Name the parasite shown.
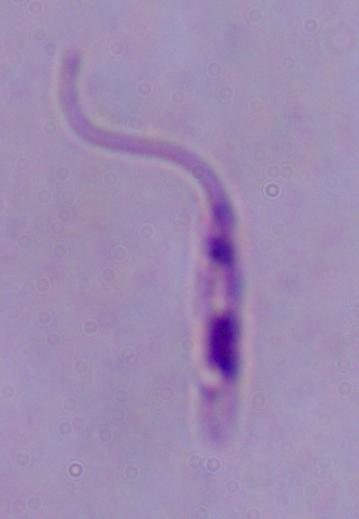
This is Leishmania.

Photomicrograph. Captured at 1000x magnification.